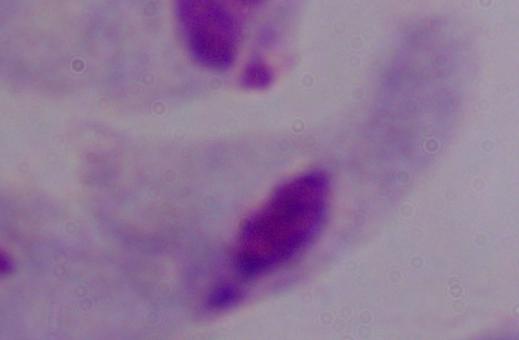
Micrograph. A trichomonad is shown. 1000x magnification.